Comment on the morphology of the red blood cells.
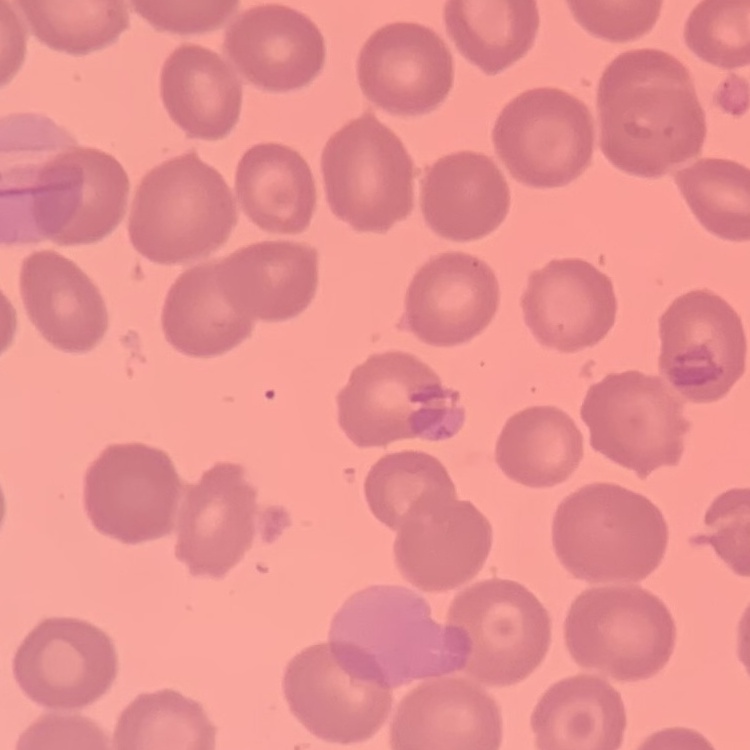

They show no rouleaux formation.

Thin blood film. Stained with either Field's or Giemsa. Square crop of a larger photomicrograph.